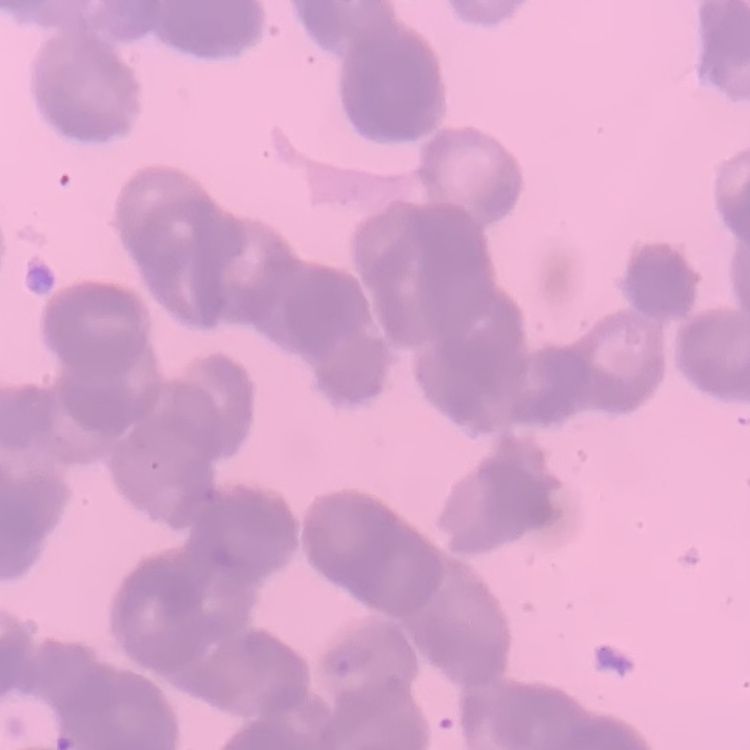
{
  "erythrocyte_morphology": "rouleaux formation",
  "preparation": "thin peripheral smear",
  "image_type": "one tile cut from a larger photomicrograph",
  "stain": "Field's or Giemsa"
}